Assess the morphology of the erythrocytes.
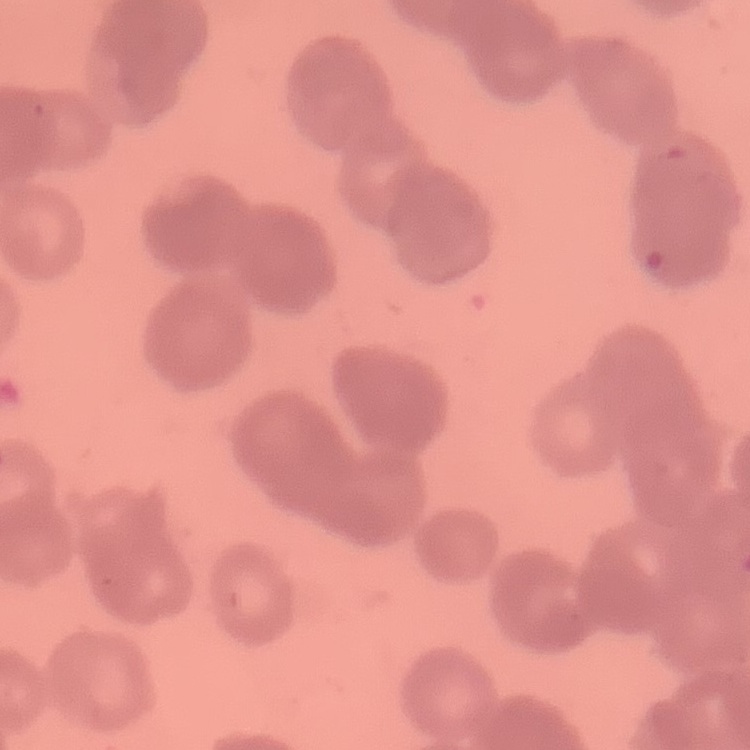
They show rouleaux formation.

Stained with either Field's or Giemsa. Square crop of a larger photomicrograph. Thin blood film.